Give the position of every Plasmodium parasite and every leukocyte.
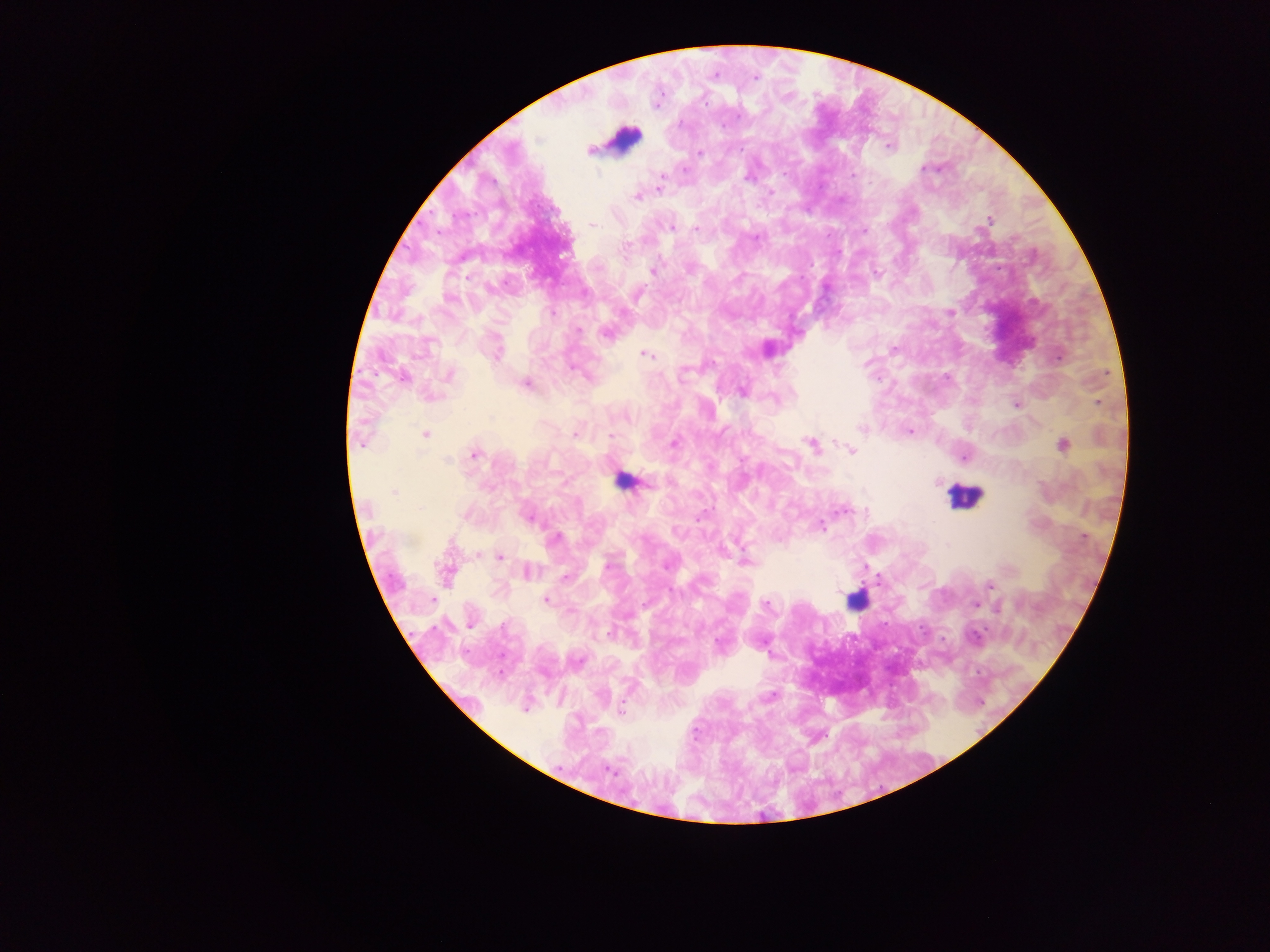

Approximate centers as (x, y) in pixels.
Plasmodium parasites: (715, 76), (756, 77), (888, 145), (590, 151), (699, 153), (924, 168), (684, 170), (783, 174), (853, 175), (662, 177), (748, 177), (659, 189), (771, 192), (637, 197), (989, 220), (593, 225), (671, 228), (696, 229), (864, 230), (755, 238), (652, 271), (876, 272), (552, 312), (950, 313), (578, 330), (606, 334), (894, 349), (497, 353), (645, 355), (1059, 358), (573, 368), (450, 374), (401, 378), (526, 383), (742, 392), (1098, 403), (1016, 405), (626, 417), (861, 429), (909, 431), (425, 434), (574, 435), (611, 436), (674, 443), (360, 444), (812, 445), (1063, 445), (851, 450), (475, 454), (964, 458), (448, 460), (393, 493), (420, 508), (843, 511), (867, 512), (528, 517), (699, 517), (822, 526), (1084, 537), (555, 538), (500, 557), (747, 562), (608, 565), (666, 567), (528, 571), (446, 574), (564, 577), (989, 585), (433, 600), (546, 601), (766, 604), (975, 604), (998, 609), (470, 624), (608, 634), (975, 636), (718, 644), (772, 697), (609, 770).
Leukocytes: (624, 139), (623, 484), (963, 496), (856, 600).

country = Ghana
field of view = single
preparation = thick blood film
image size = 1270×952 pixels
capture = mobile-phone photograph through a microscope